Outline each blood parasite and name the species.
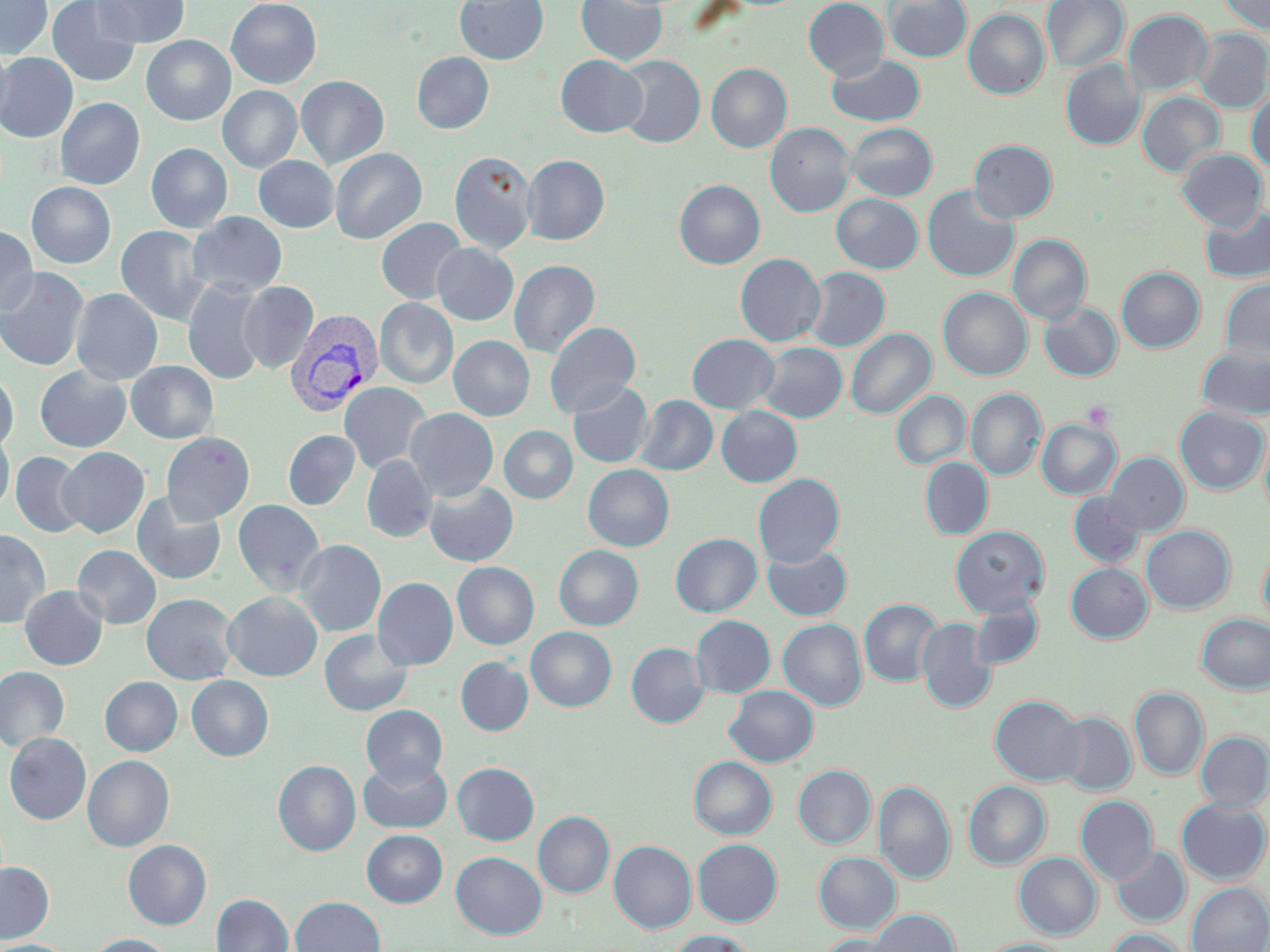

Approximate bounding boxes as (x1, y1, x2, y2) in pixels.
Plasmodium vivax-infected red blood cells: (285, 308, 383, 416).
No Plasmodium falciparum, Plasmodium ovale, Plasmodium malariae, Babesia divergens, or Trypanosoma brucei observed.

Summary:
  - Platelet locations: (1083, 399, 1116, 430)
  - Uninfected red blood cell locations: (0, 0, 53, 59), (47, 0, 141, 87), (94, 0, 190, 48), (226, 0, 321, 88), (455, 0, 548, 64), (575, 0, 668, 66), (803, 0, 889, 80), (883, 0, 971, 62), (1042, 0, 1129, 74), (1217, 0, 1270, 34), (963, 9, 1049, 99), (1123, 10, 1213, 96), (1194, 28, 1270, 113), (141, 35, 235, 126), (0, 41, 13, 131), (411, 51, 494, 134), (0, 52, 78, 142), (827, 54, 925, 126), (555, 55, 647, 138), (615, 55, 705, 148), (1061, 59, 1146, 150), (706, 63, 792, 153), (296, 75, 389, 170), (218, 85, 302, 173), (1137, 92, 1225, 177), (1246, 92, 1270, 173), (54, 97, 145, 189), (765, 123, 855, 218), (847, 123, 937, 201), (968, 139, 1057, 223), (146, 143, 232, 233), (330, 148, 427, 244), (1177, 149, 1268, 232), (449, 151, 537, 255), (522, 155, 609, 245), (253, 156, 339, 233), (674, 179, 765, 269), (26, 182, 116, 268), (922, 186, 1019, 283), (831, 194, 923, 273), (1201, 206, 1270, 283), (187, 212, 287, 298), (376, 218, 467, 305), (0, 225, 38, 317), (115, 225, 210, 325), (1008, 234, 1091, 325), (433, 243, 518, 325), (735, 253, 825, 346), (509, 259, 600, 359), (0, 266, 90, 371), (804, 267, 890, 351), (1116, 267, 1205, 353), (1219, 277, 1270, 364), (182, 279, 270, 385), (238, 281, 318, 374), (938, 287, 1032, 380), (71, 288, 162, 385), (375, 298, 458, 389), (1039, 301, 1122, 381), (544, 322, 641, 418), (846, 328, 936, 419), (687, 333, 779, 414), (449, 336, 534, 421), (757, 342, 847, 422), (1196, 345, 1270, 420), (126, 361, 218, 444), (34, 365, 131, 452), (0, 369, 19, 455), (339, 381, 432, 475), (568, 381, 653, 468), (966, 388, 1045, 481), (891, 391, 970, 469), (636, 395, 717, 476), (716, 406, 802, 487), (1174, 407, 1268, 495), (404, 408, 498, 500), (1037, 419, 1121, 499), (1260, 424, 1270, 523), (499, 426, 577, 503), (0, 430, 14, 517), (283, 430, 359, 510), (161, 432, 254, 524), (57, 447, 149, 538), (10, 451, 88, 538), (1104, 453, 1189, 536), (361, 455, 437, 542), (920, 458, 993, 540), (583, 464, 674, 551), (753, 473, 845, 567), (424, 480, 518, 566), (131, 492, 227, 585), (1068, 492, 1145, 569), (232, 498, 326, 597), (950, 525, 1050, 616), (1141, 525, 1235, 613), (0, 528, 51, 629), (670, 533, 762, 616), (294, 539, 386, 637), (762, 543, 852, 621), (1258, 544, 1270, 631), (73, 545, 161, 629), (554, 545, 643, 631), (452, 562, 539, 650), (1066, 562, 1152, 643), (373, 577, 458, 670), (20, 585, 107, 670), (223, 591, 323, 681), (141, 593, 239, 686), (859, 598, 942, 687), (969, 600, 1043, 670), (1196, 614, 1270, 694), (691, 615, 776, 698), (778, 618, 867, 711), (916, 618, 996, 713), (526, 627, 617, 711), (319, 628, 413, 717), (626, 642, 709, 728), (455, 656, 533, 736), (0, 666, 69, 752), (186, 675, 274, 762), (100, 677, 182, 756), (725, 685, 818, 767), (1130, 687, 1209, 780), (990, 695, 1086, 785), (361, 705, 448, 786), (1057, 712, 1138, 796), (1196, 731, 1270, 811), (4, 732, 91, 824), (83, 755, 174, 852), (358, 756, 453, 834), (689, 756, 776, 839), (273, 759, 360, 856), (452, 762, 539, 845), (793, 765, 875, 848), (873, 780, 955, 885), (963, 781, 1050, 869), (1076, 796, 1158, 883), (1176, 798, 1270, 885), (534, 811, 614, 898), (362, 829, 447, 907), (123, 839, 212, 930), (693, 839, 782, 926), (609, 840, 696, 933), (1111, 846, 1190, 928), (451, 852, 547, 940), (814, 852, 901, 934), (1014, 853, 1101, 939), (0, 862, 54, 942), (1186, 882, 1270, 952), (212, 894, 293, 952), (291, 896, 386, 952), (867, 909, 960, 952), (1104, 928, 1190, 952), (668, 929, 757, 952), (87, 934, 174, 952), (817, 934, 904, 952), (979, 938, 1073, 952), (0, 939, 74, 952)
  - Slide-level diagnosis: Plasmodium vivax
  - Stain: May-Grünwald-Giemsa
  - Field of view: single
  - Preparation: thin blood smear
  - Image size: 1270×952 pixels
  - Magnification: 1000x
  - Modality: optical microscopy